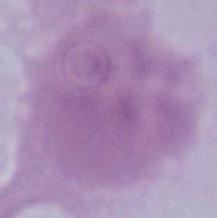

modality: micrograph
identification: red blood cell
magnification: 1000x